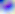

{
  "modality": "micrograph",
  "magnification": "400x",
  "identification": "Toxoplasma gondii"
}